Name the blood parasite species.
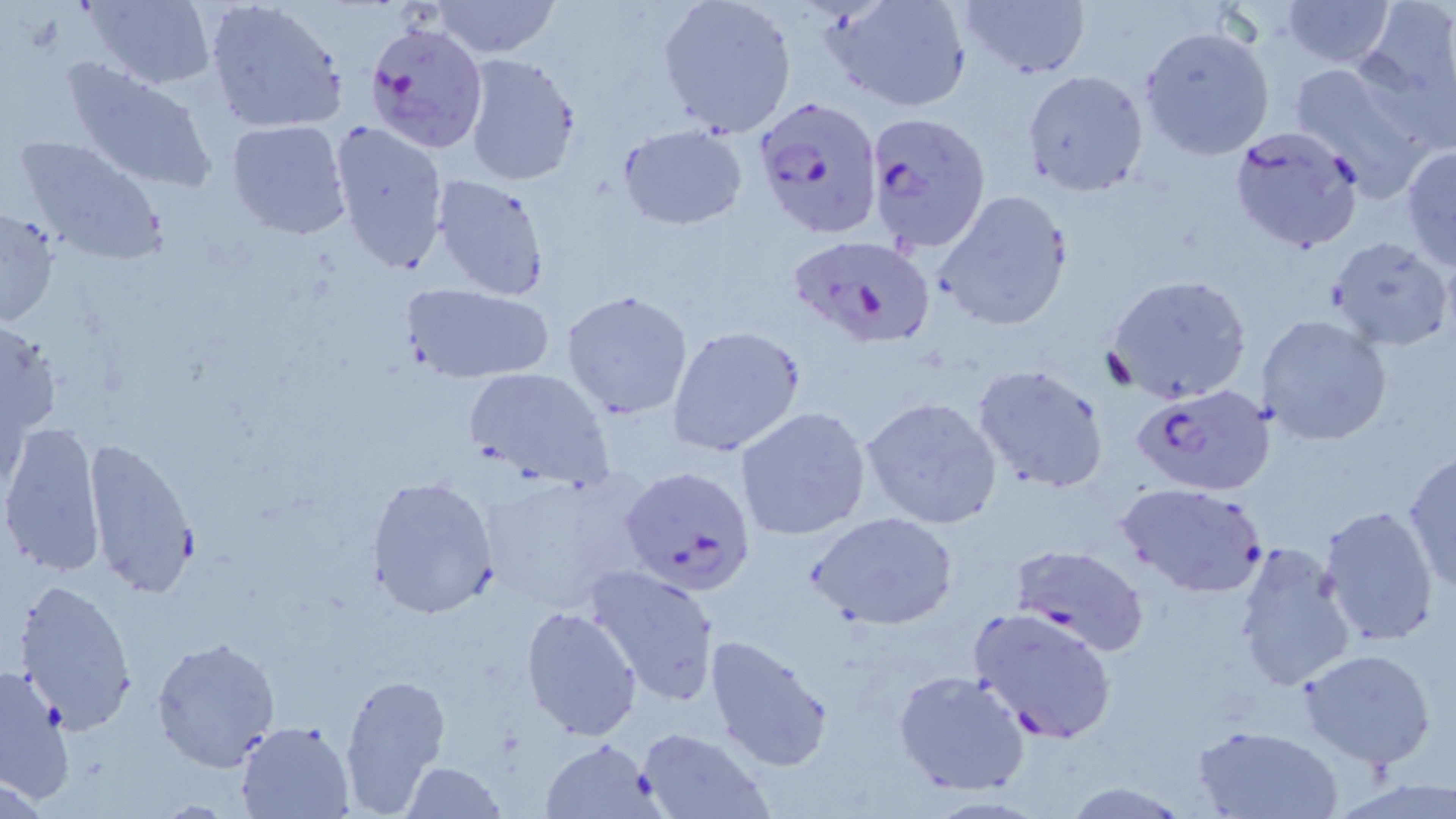
Plasmodium falciparum.

modality = optical microscopy
Plasmodium falciparum-infected red blood cell locations = approximate bounding boxes as (x1,y1)-(x2,y2) corner pairs in pixels: (362,18)-(488,153), (751,94)-(883,241), (864,110)-(993,256), (1224,124)-(1369,255), (787,233)-(936,347), (1133,383)-(1276,496), (621,465)-(758,597), (1008,543)-(1150,655), (968,605)-(1118,744)
magnification = 1000x
preparation = thin blood smear
uninfected red blood cell locations = approximate bounding boxes as (x1,y1)-(x2,y2) corner pairs in pixels: (204,0)-(348,134), (435,0)-(560,58), (657,0)-(799,138), (957,0)-(1090,80), (1280,0)-(1398,68), (80,1)-(219,89), (824,1)-(971,112), (1355,5)-(1454,132), (1140,24)-(1277,160), (459,53)-(583,188), (60,57)-(219,195), (1285,59)-(1439,198), (1021,68)-(1148,196), (328,119)-(450,275), (226,120)-(352,239), (617,124)-(747,229), (15,133)-(170,267), (1400,145)-(1456,270), (429,174)-(552,300), (933,189)-(1074,332), (0,206)-(60,329), (1327,236)-(1452,351), (1104,274)-(1252,406), (400,283)-(557,383), (560,290)-(695,420), (1256,313)-(1392,446), (666,325)-(806,458), (973,364)-(1110,494), (461,366)-(613,489), (859,395)-(1004,530), (734,407)-(874,543), (1,421)-(106,579), (82,434)-(200,601), (1403,451)-(1456,595), (479,471)-(646,611), (366,475)-(501,620), (1118,482)-(1268,599), (1317,504)-(1439,649), (810,511)-(959,630), (1231,538)-(1360,697), (584,565)-(722,705), (14,577)-(139,737), (519,605)-(641,742), (703,633)-(834,774), (150,635)-(281,774), (1297,647)-(1437,768), (1,663)-(74,799), (337,670)-(453,816), (893,670)-(1030,796), (236,721)-(356,818), (1192,722)-(1343,818), (635,727)-(774,818), (539,737)-(665,818), (401,760)-(507,819), (1059,781)-(1190,817)
image size = 1456×819 pixels
stain = May-Grünwald-Giemsa
field of view = single